Locate and identify every blood parasite.
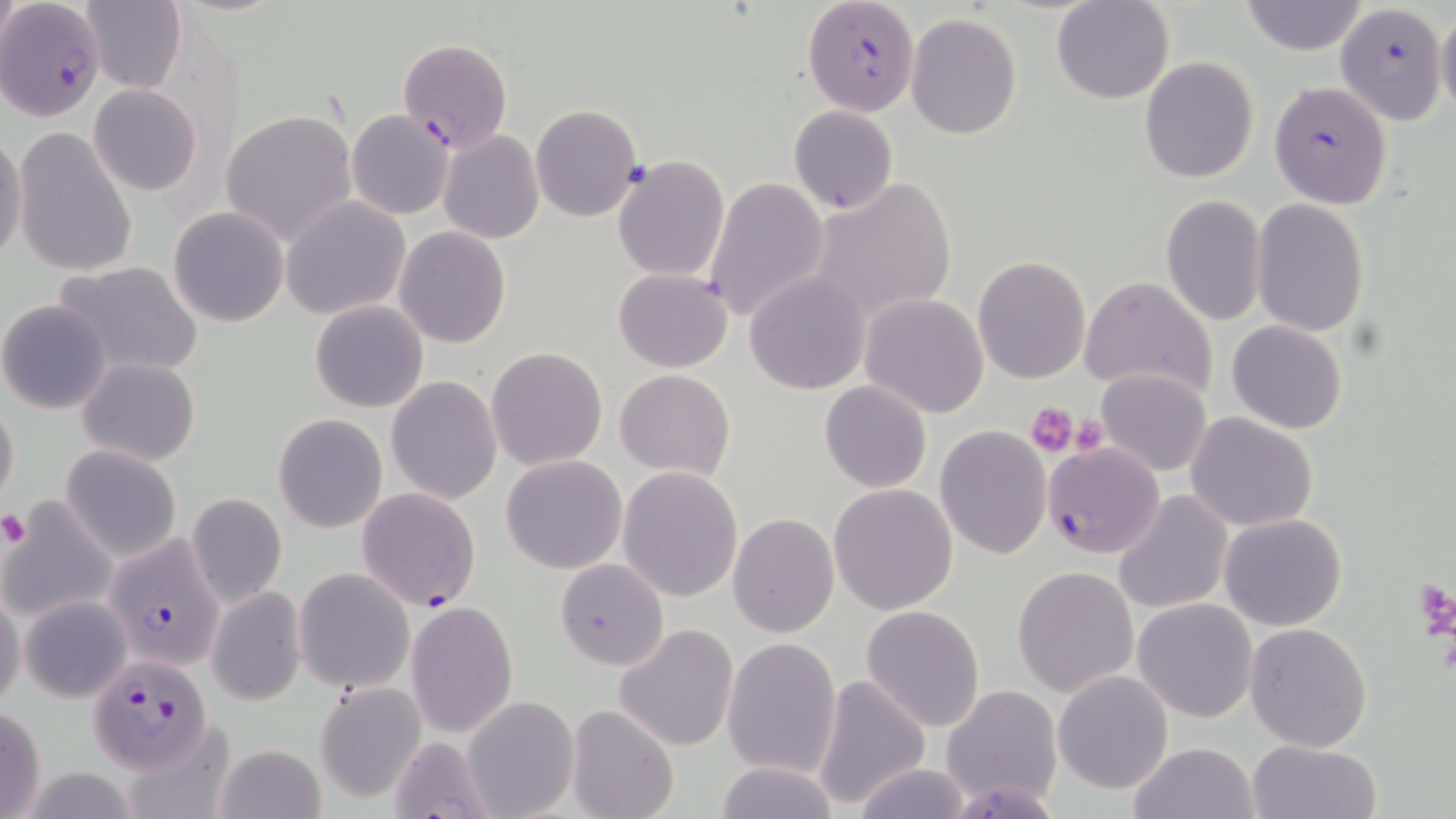

Approximate bounding boxes as [x1, y1, x2, y2] in pixels.
Plasmodium falciparum-infected red blood cells: [803, 0, 920, 115], [0, 1, 107, 121], [1335, 3, 1447, 126], [398, 36, 512, 154], [1269, 81, 1394, 210], [1042, 441, 1165, 561], [357, 486, 481, 611], [103, 532, 224, 670], [87, 654, 215, 772].
No Plasmodium ovale, Plasmodium malariae, Plasmodium vivax, Babesia divergens, or Trypanosoma brucei observed.

Summary:
  - Platelet locations: [1026, 402, 1078, 457], [1068, 414, 1110, 454], [0, 513, 31, 547], [1417, 578, 1456, 646]
  - Uninfected red blood cell locations: [1, 0, 20, 67], [1052, 0, 1174, 104], [79, 1, 186, 92], [1239, 1, 1368, 55], [1435, 7, 1456, 120], [905, 13, 1024, 140], [1139, 56, 1258, 184], [89, 83, 202, 197], [531, 103, 641, 222], [788, 105, 897, 214], [221, 109, 359, 249], [346, 109, 455, 221], [11, 127, 139, 279], [439, 130, 544, 244], [0, 131, 26, 266], [612, 154, 729, 282], [702, 174, 831, 325], [810, 177, 956, 325], [1160, 194, 1266, 326], [282, 196, 411, 320], [1252, 199, 1368, 336], [168, 206, 289, 327], [393, 226, 511, 349], [972, 255, 1091, 385], [54, 261, 204, 379], [615, 269, 732, 373], [745, 272, 871, 394], [1079, 275, 1217, 400], [858, 293, 989, 419], [0, 300, 113, 415], [309, 300, 429, 414], [1227, 320, 1347, 434], [487, 347, 608, 471], [76, 357, 201, 465], [615, 368, 734, 480], [1096, 369, 1212, 477], [386, 376, 502, 506], [820, 380, 931, 493], [0, 399, 20, 510], [273, 413, 387, 533], [1187, 413, 1317, 532], [934, 425, 1051, 558], [61, 445, 181, 562], [501, 455, 627, 574], [616, 466, 743, 602], [829, 483, 959, 615], [1114, 490, 1233, 614], [186, 492, 287, 609], [1, 499, 114, 625], [727, 513, 840, 638], [1218, 513, 1347, 630], [554, 559, 668, 672], [1013, 565, 1138, 697], [293, 567, 414, 694], [582, 582, 711, 719], [207, 585, 306, 706], [0, 588, 25, 713], [19, 595, 132, 702], [1133, 598, 1257, 722], [406, 601, 517, 736], [861, 604, 985, 732], [1245, 621, 1373, 752], [614, 623, 740, 752], [722, 637, 843, 778], [1053, 671, 1174, 794], [808, 674, 931, 812], [316, 683, 426, 801], [942, 684, 1064, 809], [462, 695, 578, 819], [566, 703, 678, 819], [0, 704, 47, 819], [383, 734, 499, 818], [1245, 739, 1383, 819], [1127, 741, 1260, 819], [213, 743, 327, 819], [712, 759, 842, 819], [849, 763, 978, 819]
  - Slide-level diagnosis: Plasmodium falciparum
  - Image size: 1456×819 pixels
  - Preparation: thin blood film
  - Modality: light microscopy
  - Magnification: 1000x
  - Stain: May-Grünwald-Giemsa
  - Field of view: single